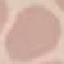
Summary:
  - Result: no malaria parasites detected
  - Capture: smartphone through the microscope eyepiece
  - Preparation: thin blood smear
  - Stain: Giemsa
  - Image type: cell patch, automatically extracted from a larger field of view and resized to 64 × 64 pixels